Give the position of every Plasmodium parasite.
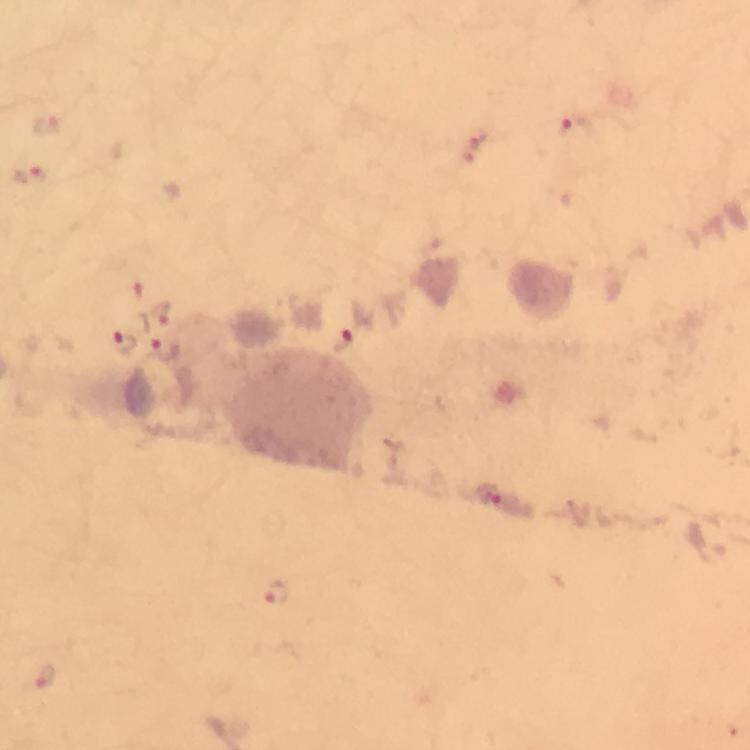

Approximate centers as {x, y} in pixels.
Plasmodium parasites: {47, 127}, {574, 129}, {478, 144}, {31, 176}, {136, 288}, {160, 314}, {350, 340}, {121, 342}, {167, 350}, {491, 495}, {278, 592}, {45, 676}.

Immersion oil applied. Thick blood film. At 100x magnification. A crop from one field of view. From a malaria diagnostic workup. Giemsa-stained preparation. Photographed with a smartphone mounted on the microscope. Image is 750×750 pixels.